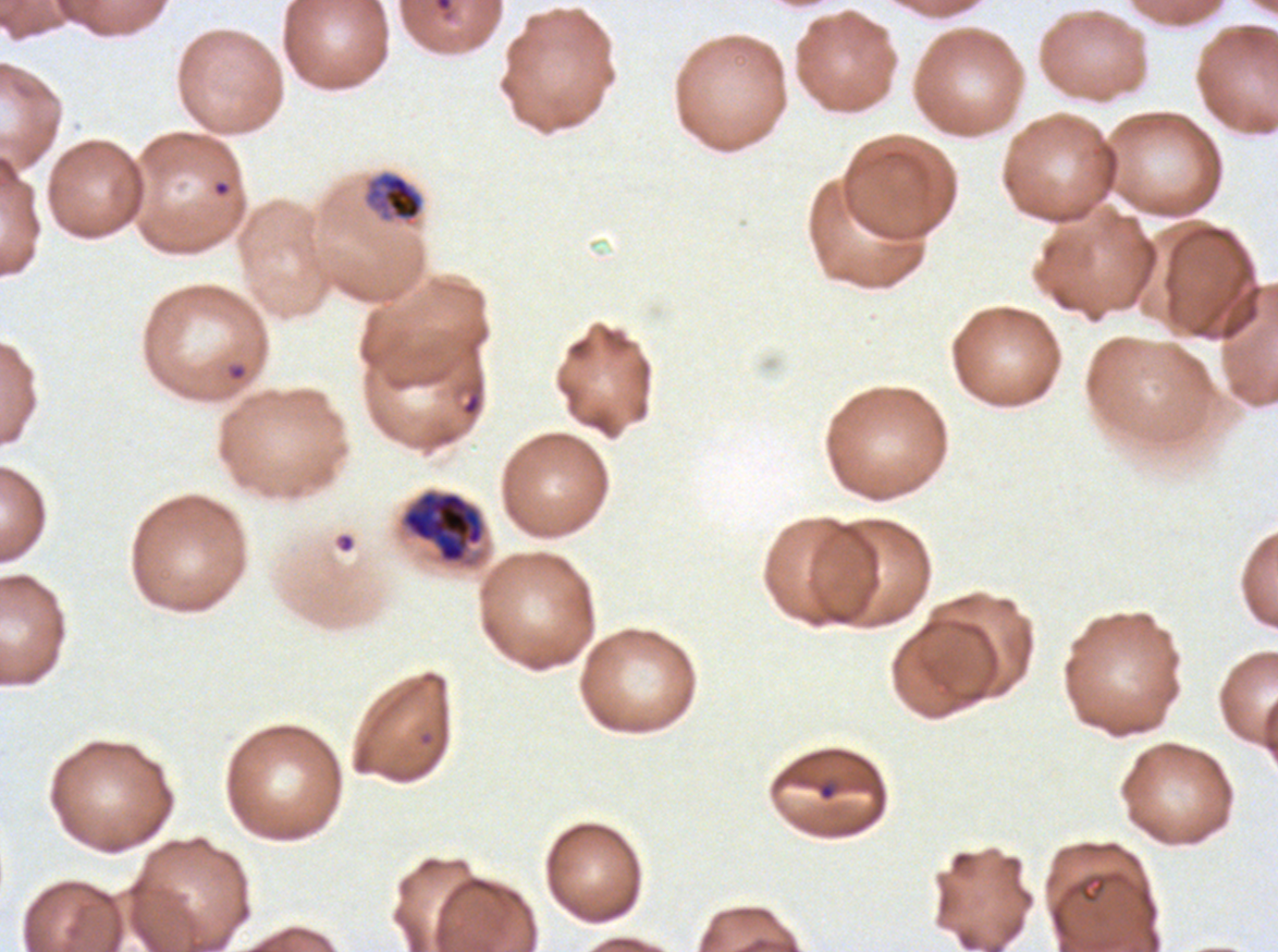
Approximate bounding boxes as [x1, y1, x2, y2] in pixels.
Summary:
  - Mid trophozoite locations: [363, 170, 424, 225]
  - Debris locations: [433, 0, 453, 13]
  - Early schizont locations: [403, 492, 484, 563]
  - Ring locations: [212, 179, 231, 198], [461, 391, 482, 417], [817, 781, 837, 801]
  - Life-cycle stages observed: ring, mid trophozoite, early schizont
  - Stain: Giemsa
  - Preparation: thin blood smear
  - Field of view: sub-image separated from a larger composite
  - Specimen: ex-vivo Plasmodium falciparum culture from a patient in The Gambia, grown for 24 to 48 hours
  - Image size: 1278×952 pixels